State which parasite is depicted.
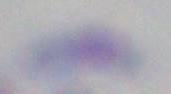

This is Toxoplasma gondii.

Micrograph. Captured at 1000x magnification.